Report the malaria status of this cell.
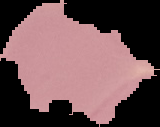

It is uninfected.

preparation = thin blood film
image type = segmented cell region on a black background
image size = 160×127 pixels